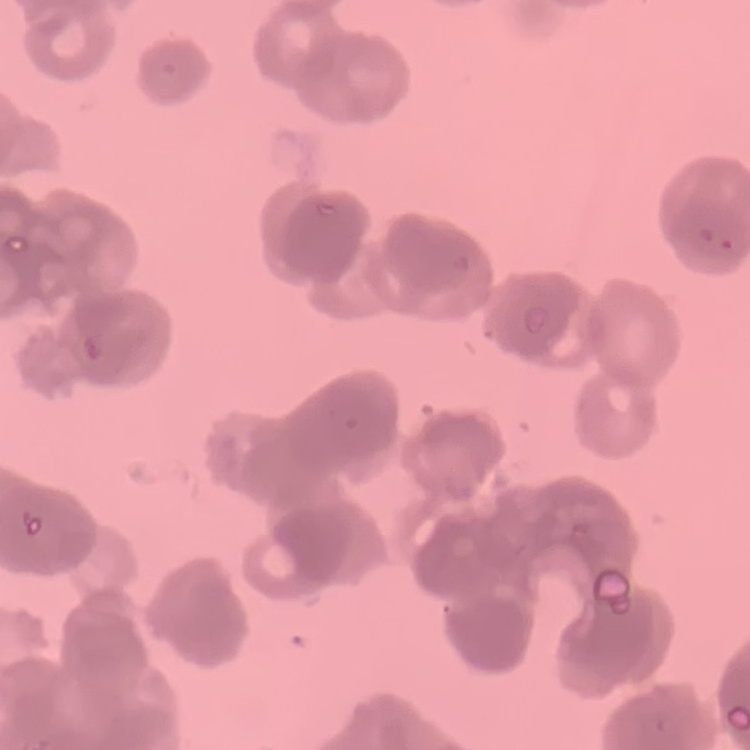

Summary:
  - Erythrocyte morphology: rouleaux formation
  - Image type: one tile cut from a larger photomicrograph
  - Stain: Field's or Giemsa
  - Preparation: thin peripheral smear